Point out every Plasmodium parasite.
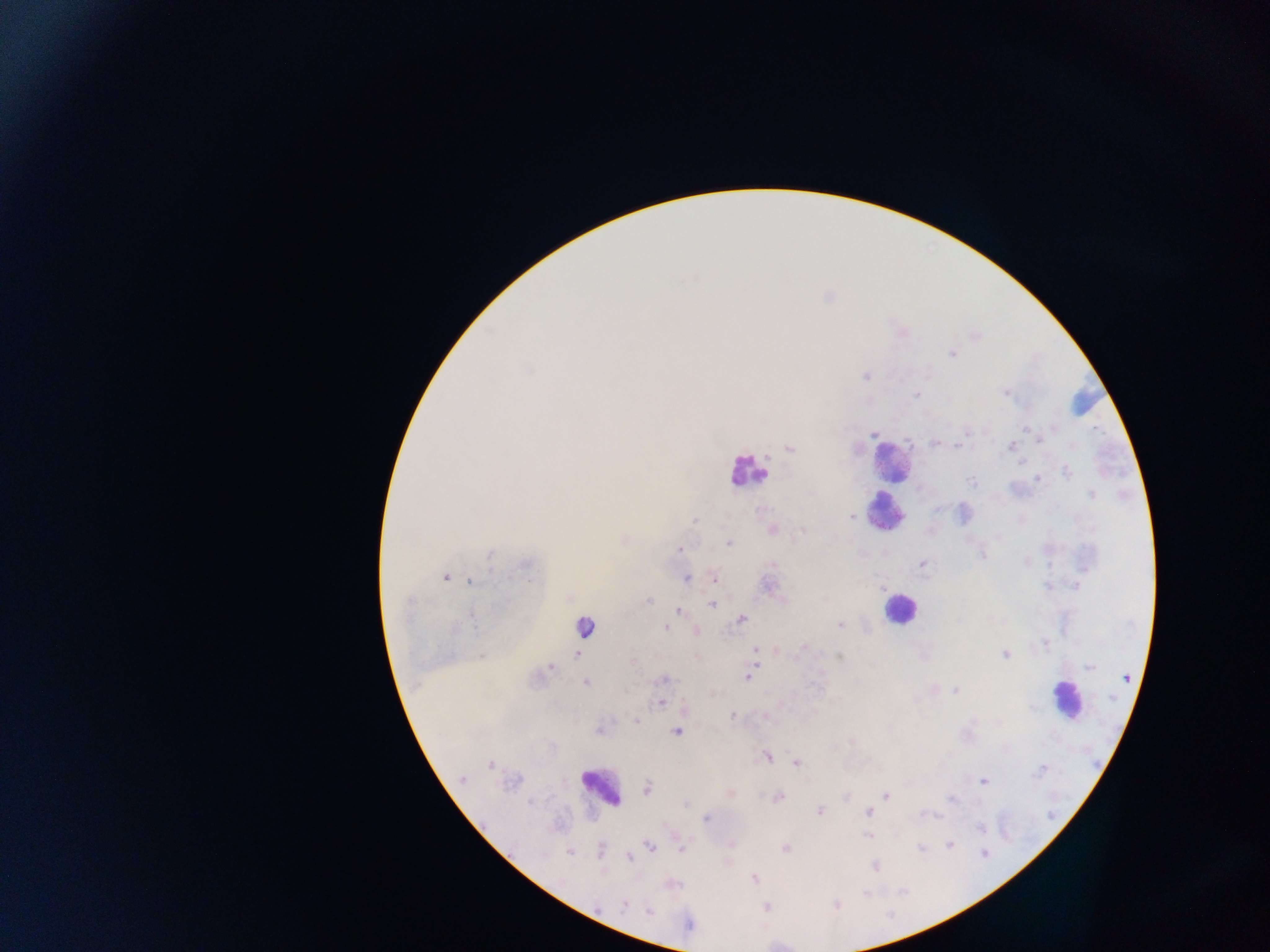

Approximate centers as x y in pixels.
Plasmodium parasites: 696 277; 975 337; 950 354; 529 372; 864 378; 1003 393; 915 396; 1026 429; 1055 429; 873 434; 1038 440; 935 442; 1071 444; 958 446; 790 447; 1008 447; 1022 462; 1066 472; 1037 480; 971 481; 1090 495; 852 516; 694 521; 623 540; 728 544; 677 550; 490 556; 982 556; 1028 561; 923 565; 526 567; 1050 569; 446 577; 713 577; 688 579; 472 581; 1076 584; 1048 587; 648 601; 408 604; 711 605; 678 609; 741 619; 472 620; 839 624; 583 628; 666 629; 697 631; 1045 642; 755 648; 803 649; 1005 654; 481 655; 577 656; 838 656; 550 667; 1089 669; 749 677; 662 680; 585 684; 956 690; 660 704; 1034 708; 732 714; 637 720; 677 732; 768 758; 795 764; 490 765; 1042 767; 461 779; 984 782; 510 784; 648 791; 780 796; 886 796; 953 798; 530 804; 686 804; 821 811; 867 813; 929 814; 937 816; 705 818; 981 828; 868 838; 950 843; 649 846; 786 848; 599 849; 682 850; 920 850; 569 853; 983 853; 629 860; 876 866; 867 893; 622 904; 836 905; 767 907; 647 910.

preparation = thick blood film
country = Ghana
capture = mobile-phone photograph through a microscope
leukocyte locations = approximate centers as x y in pixels: 892 464; 889 507; 897 611; 1060 699; 600 783
field of view = single
image size = 1270×952 pixels